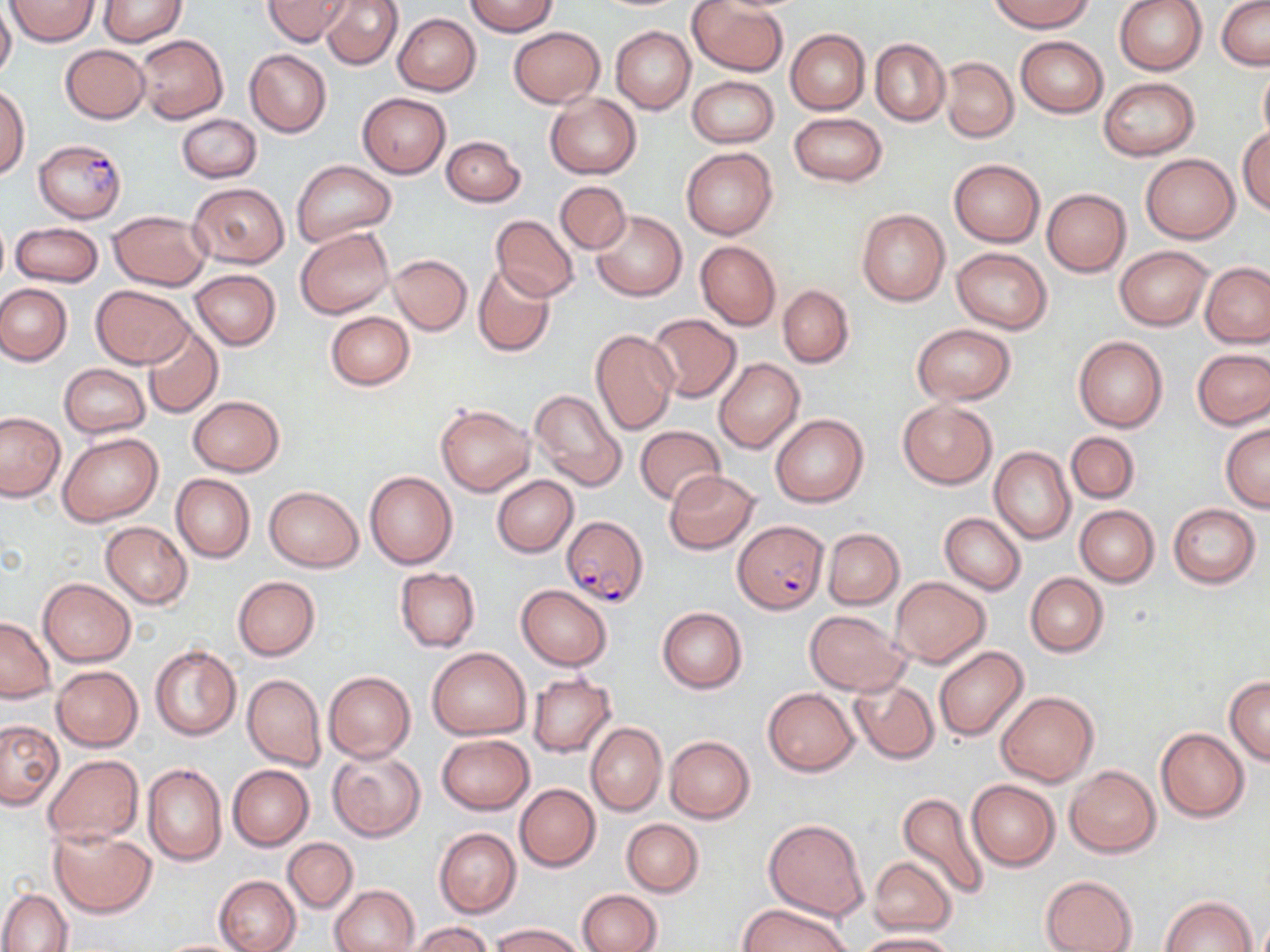
Summary:
  - Coordinate format: approximate bounding boxes as [x1, y1, x2, y2] in pixels
  - Uninfected red blood cell locations: [6, 0, 99, 46], [97, 0, 186, 46], [263, 0, 350, 46], [320, 0, 403, 69], [989, 0, 1094, 31], [1114, 0, 1209, 76], [465, 1, 557, 36], [689, 1, 788, 76], [1218, 1, 1270, 71], [0, 5, 15, 82], [392, 13, 481, 95], [509, 26, 603, 107], [612, 26, 696, 113], [786, 29, 870, 114], [136, 34, 228, 123], [1015, 36, 1108, 118], [870, 38, 949, 127], [60, 44, 150, 123], [245, 49, 331, 136], [941, 57, 1018, 143], [1258, 65, 1270, 149], [687, 75, 778, 148], [1098, 77, 1199, 160], [0, 87, 29, 178], [357, 92, 452, 178], [545, 92, 642, 179], [789, 112, 888, 187], [177, 113, 261, 182], [1238, 126, 1270, 216], [442, 136, 525, 207], [681, 146, 778, 240], [1141, 153, 1240, 243], [949, 158, 1044, 246], [291, 161, 396, 244], [555, 181, 631, 254], [189, 182, 288, 267], [1042, 188, 1131, 277], [856, 208, 949, 305], [108, 210, 211, 291], [592, 210, 686, 301], [490, 215, 579, 301], [10, 222, 103, 287], [295, 228, 393, 318], [695, 240, 780, 331], [1115, 245, 1213, 329], [952, 247, 1053, 333], [388, 255, 472, 335], [1200, 262, 1269, 347], [473, 264, 556, 358], [189, 270, 280, 350], [0, 283, 72, 365], [92, 285, 193, 368], [777, 285, 854, 367], [325, 311, 415, 389], [645, 313, 742, 404], [143, 323, 223, 418], [911, 324, 1016, 404], [590, 330, 680, 435], [1073, 336, 1167, 433], [1192, 347, 1270, 430], [713, 358, 805, 454], [58, 363, 150, 438], [529, 388, 628, 493], [188, 396, 284, 477], [897, 399, 997, 488], [434, 402, 535, 496], [0, 412, 65, 501], [771, 414, 869, 507], [1220, 423, 1270, 513], [635, 425, 726, 505], [59, 432, 162, 525], [1066, 432, 1140, 504], [990, 446, 1075, 545], [664, 470, 759, 553], [365, 471, 456, 569], [170, 473, 255, 563], [492, 475, 578, 557], [263, 486, 364, 572], [1168, 503, 1261, 588], [1074, 504, 1158, 587], [939, 512, 1026, 595], [101, 522, 192, 609], [823, 528, 903, 608], [395, 567, 481, 651], [1025, 573, 1109, 657], [233, 575, 320, 660], [889, 577, 990, 667], [39, 578, 136, 667], [516, 585, 613, 670], [657, 606, 746, 693], [805, 611, 909, 695], [0, 616, 55, 702], [149, 645, 241, 741], [933, 646, 1029, 741], [428, 647, 530, 740], [52, 666, 142, 751], [324, 670, 415, 762], [527, 673, 616, 757], [242, 674, 326, 771], [1224, 676, 1270, 765], [850, 677, 939, 764], [764, 687, 859, 775], [996, 691, 1098, 786], [1, 720, 65, 810], [585, 721, 666, 816], [1156, 727, 1250, 821], [437, 734, 534, 814], [664, 736, 755, 824], [327, 749, 425, 842], [43, 754, 142, 847], [143, 764, 227, 866], [228, 764, 314, 850], [1066, 765, 1160, 857], [966, 779, 1060, 870], [515, 783, 600, 871], [896, 790, 993, 901], [764, 817, 871, 921], [621, 819, 703, 897], [49, 824, 157, 918], [434, 828, 521, 918], [283, 838, 357, 913], [869, 858, 956, 936], [1040, 874, 1138, 952], [215, 875, 300, 952], [331, 885, 420, 952], [0, 889, 72, 952], [578, 889, 662, 952], [1161, 895, 1257, 951], [739, 903, 851, 952], [409, 922, 495, 952], [494, 923, 583, 952], [860, 932, 957, 952], [155, 939, 251, 952]
  - Plasmodium falciparum-infected red blood cell locations: [33, 138, 126, 222], [560, 515, 650, 608], [734, 517, 828, 613]
  - Slide-level diagnosis: Plasmodium falciparum
  - Modality: optical microscopy
  - Field of view: one of a larger specimen
  - Preparation: thin blood smear
  - Image size: 1270×952 pixels
  - Magnification: 1000x
  - Stain: May-Grünwald-Giemsa